Assess this cell for malaria.
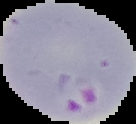

Parasitized.

Summary:
  - Image size: 136×124 pixels
  - Preparation: thin blood smear
  - Image type: segmented cell region on a black background